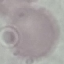

{
  "result": "negative for malaria parasites",
  "preparation": "thin blood smear",
  "capture": "smartphone camera at the microscope eyepiece",
  "image_type": "automatically extracted cell patch, resized to 64 × 64 pixels",
  "stain": "Giemsa"
}